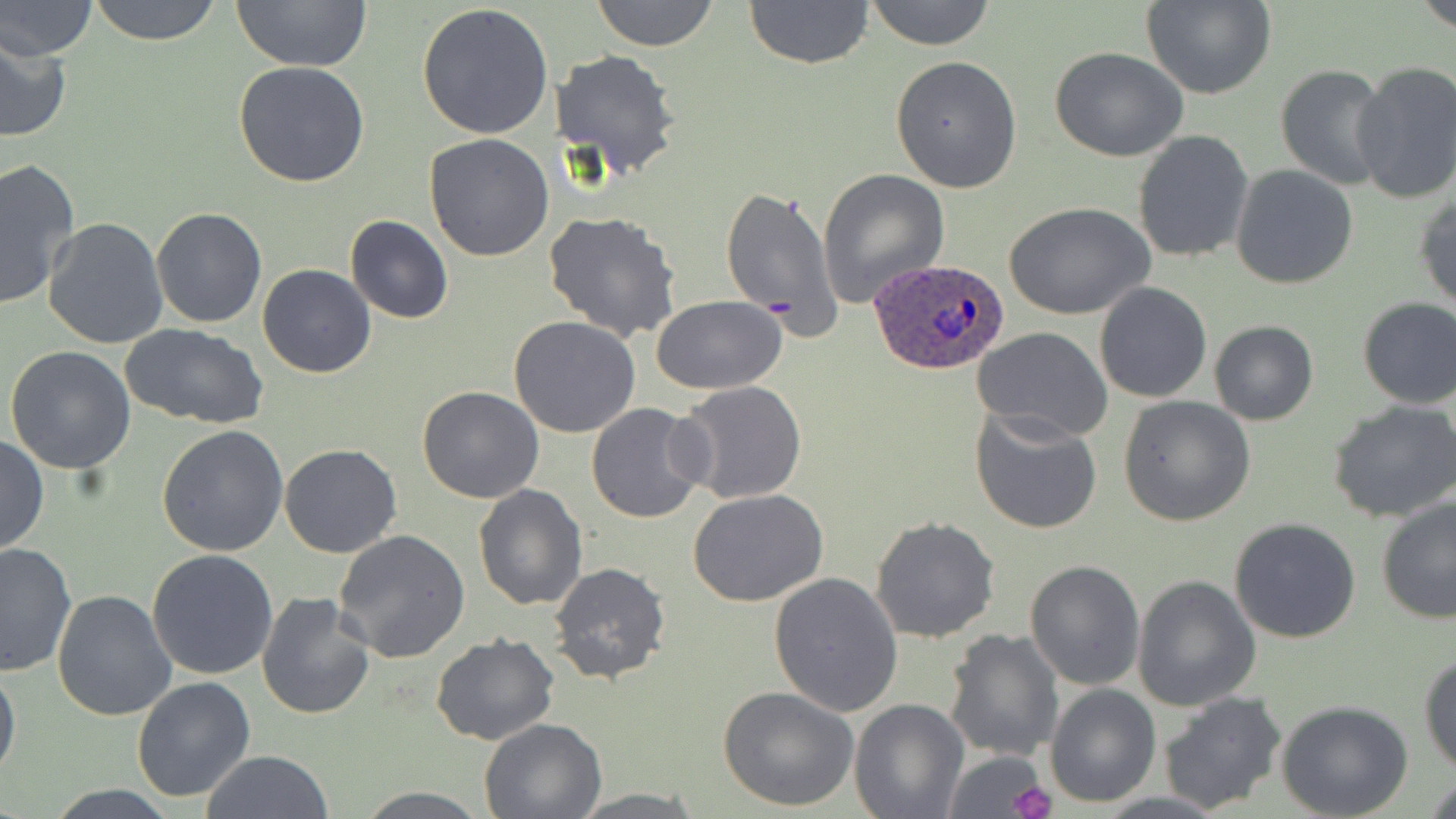
Summary:
  - Coordinate format: approximate bounding boxes as (x1, y1, x2, y2) in pixels
  - Platelet locations: (1010, 781, 1056, 819)
  - Plasmodium ovale-infected red blood cell locations: (868, 257, 1010, 374)
  - Uninfected red blood cell locations: (2, 0, 99, 60), (87, 0, 225, 46), (232, 0, 371, 72), (591, 0, 719, 50), (743, 0, 875, 69), (863, 0, 996, 50), (1417, 0, 1456, 34), (1141, 1, 1278, 100), (416, 2, 554, 142), (0, 36, 73, 143), (1048, 46, 1190, 163), (551, 48, 681, 179), (890, 55, 1023, 193), (1351, 60, 1455, 204), (233, 62, 371, 187), (1275, 64, 1393, 189), (1133, 130, 1254, 263), (424, 133, 555, 261), (0, 157, 82, 308), (1229, 164, 1358, 289), (817, 167, 950, 307), (720, 184, 843, 337), (1413, 192, 1456, 311), (1007, 202, 1154, 320), (152, 208, 268, 329), (543, 210, 682, 342), (345, 215, 453, 324), (42, 217, 168, 352), (258, 264, 377, 379), (1094, 282, 1212, 403), (651, 295, 787, 395), (1357, 296, 1455, 409), (508, 317, 641, 439), (1209, 319, 1318, 425), (120, 323, 268, 428), (972, 328, 1113, 443), (4, 345, 136, 473), (673, 381, 808, 504), (417, 385, 545, 502), (1119, 396, 1255, 525), (1328, 398, 1456, 522), (585, 402, 710, 522), (970, 406, 1104, 534), (156, 424, 289, 557), (0, 435, 47, 555), (278, 443, 402, 558), (474, 482, 588, 610), (688, 491, 828, 607), (1377, 496, 1456, 625), (1230, 516, 1362, 643), (871, 517, 1000, 642), (332, 529, 471, 663), (0, 542, 76, 677), (147, 550, 279, 681), (1025, 559, 1145, 689), (550, 562, 670, 683), (768, 572, 904, 717), (1132, 573, 1261, 711), (52, 589, 176, 723), (256, 593, 375, 720), (943, 627, 1067, 762), (432, 634, 560, 747), (1419, 652, 1456, 775), (0, 658, 21, 783), (131, 676, 256, 803), (1045, 684, 1160, 806), (718, 685, 859, 812), (1159, 690, 1287, 813), (849, 697, 969, 819), (1277, 700, 1414, 819), (477, 718, 605, 819), (941, 748, 1050, 819), (201, 750, 331, 819), (1423, 775, 1456, 819), (350, 787, 495, 818), (564, 789, 712, 817)
  - Slide-level diagnosis: Plasmodium ovale
  - Preparation: thin blood film
  - Image size: 1456×819 pixels
  - Field of view: one of a larger specimen
  - Magnification: 1000x
  - Stain: May-Grünwald-Giemsa
  - Modality: light microscopy